Classify this cell by malaria status.
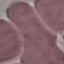

Uninfected.

Cell patch, automatically extracted from a larger field of view and resized to 64 × 64 pixels. Giemsa stain. Photographed with a smartphone camera at the microscope eyepiece. Thin blood film.